Name the parasite shown.
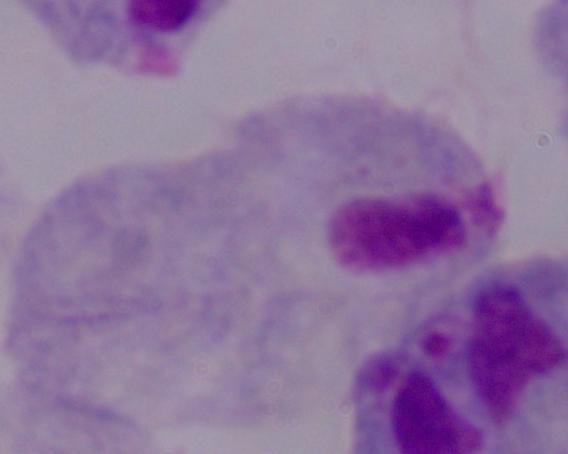
A trichomonad.

Summary:
  - Modality: photomicrograph
  - Magnification: 1000x